Describe the morphology of the erythrocytes.
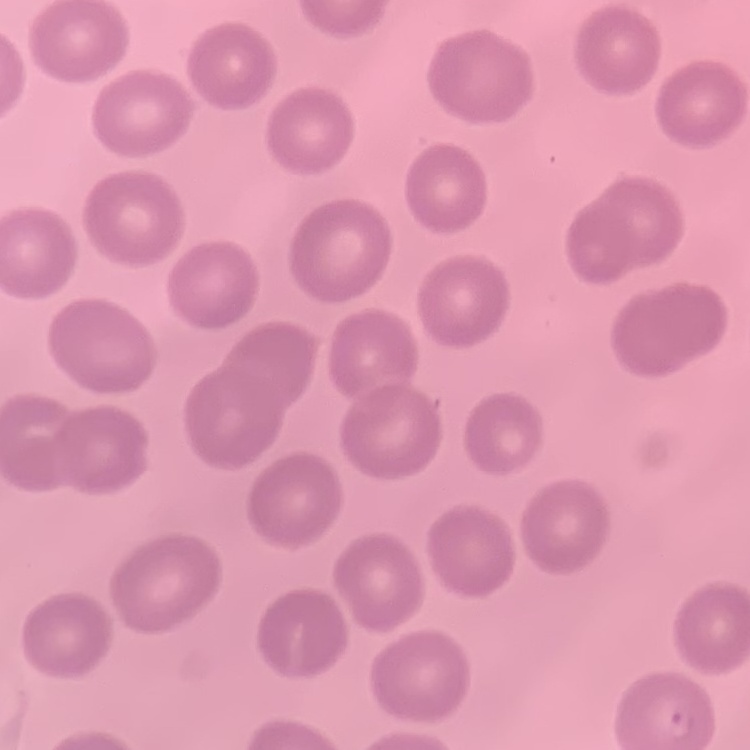

They show no rouleaux formation.

Stained with either Field's or Giemsa. Square crop of a larger photomicrograph. Thin blood smear.